Report the malaria status of this cell.
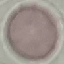

It is uninfected.

Thin smear of blood. Automatically extracted cell patch, resized to 64 × 64 pixels. Giemsa-stained preparation. Photographed with a smartphone camera at the microscope eyepiece.